State which cell type is depicted.
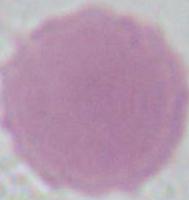

This is an erythrocyte.

Summary:
  - Magnification: 1000x
  - Modality: photomicrograph